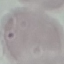

Summary:
  - Result: no malaria parasites seen
  - Image type: automatically extracted cell patch, resized to 64 × 64 pixels
  - Preparation: thin blood smear
  - Capture: smartphone through the microscope eyepiece
  - Stain: Giemsa